Classify this cell by malaria status.
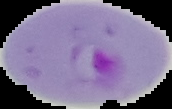

It is parasitized.

image_type: cell region segmented out of the field of view; surrounding area masked to black
image_size: 172×109 pixels
preparation: thin blood film